Classify this cell by malaria status.
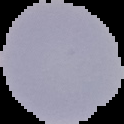
It is uninfected.

Segmented cell region on a black background. Image is 124×124 pixels. From a thin blood film.